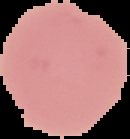

image size = 130×139 pixels
result = no malaria parasites detected
preparation = thin blood film
image type = cell region segmented out of the field of view; surrounding area masked to black